Identify the blood parasite species.
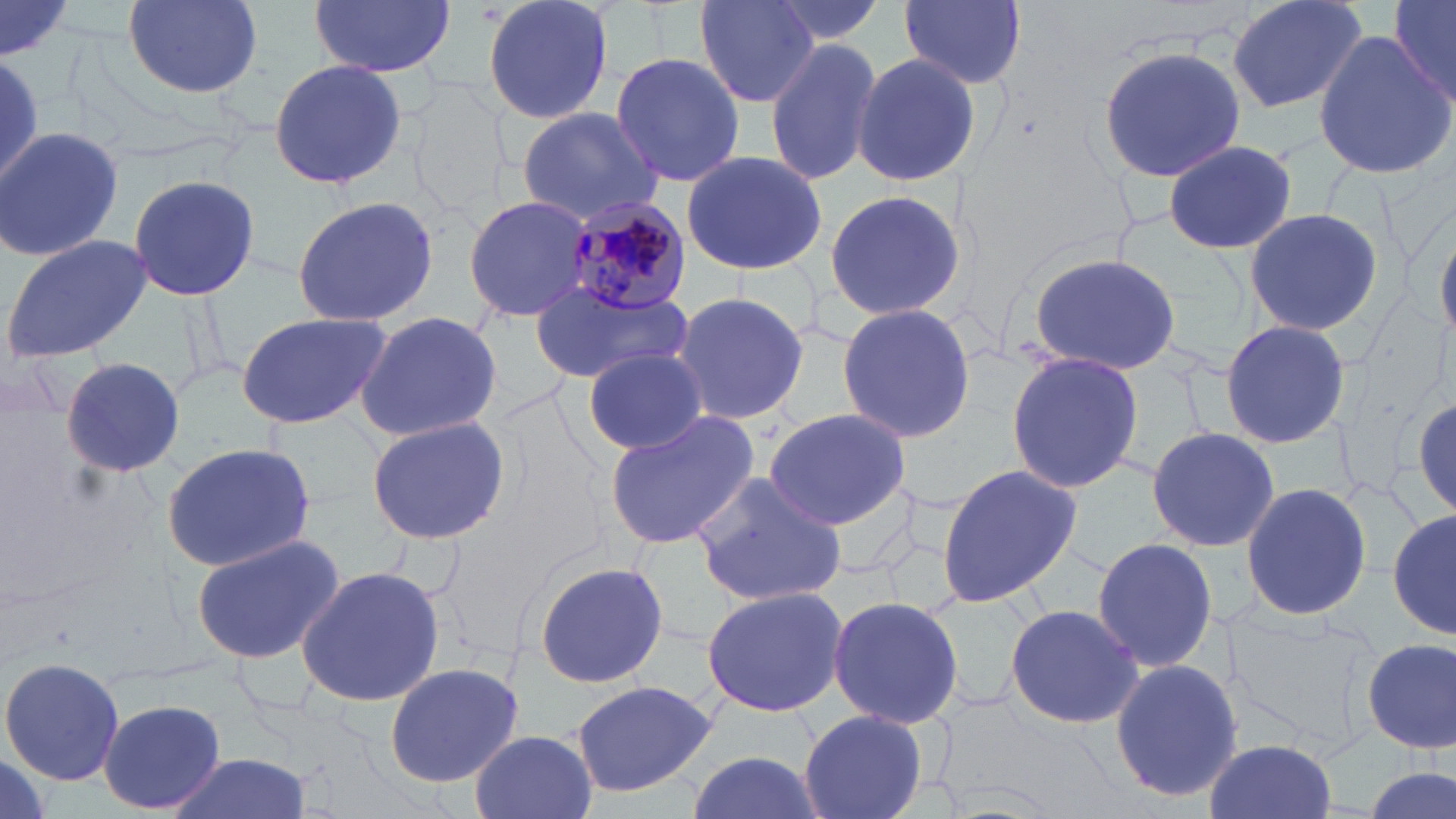

Plasmodium malariae.

Approximate bounding boxes as (x1, y1, x2, y2) in pixels. Plasmodium malariae-infected red blood cell locations: (567, 203, 692, 315). Uninfected red blood cell locations: (481, 0, 616, 127), (763, 0, 888, 48), (900, 0, 1027, 89), (1225, 0, 1372, 115), (1388, 0, 1456, 108), (121, 1, 262, 100), (310, 1, 453, 78), (697, 1, 816, 108), (0, 2, 74, 63), (1313, 32, 1455, 176), (765, 36, 882, 185), (1099, 47, 1246, 180), (609, 50, 744, 186), (851, 53, 984, 188), (266, 59, 407, 191), (515, 104, 663, 226), (1, 126, 125, 263), (1161, 138, 1299, 257), (680, 149, 830, 278), (127, 173, 261, 303), (827, 187, 968, 324), (466, 194, 593, 322), (291, 196, 440, 326), (1241, 206, 1388, 339), (1435, 225, 1455, 342), (1, 235, 153, 363), (1026, 252, 1183, 376), (531, 280, 694, 385), (667, 292, 809, 428), (836, 303, 979, 444), (353, 310, 505, 442), (236, 312, 392, 429), (1220, 319, 1350, 447), (1004, 350, 1146, 492), (583, 351, 709, 453), (61, 358, 186, 476), (1407, 388, 1456, 524), (763, 407, 914, 530), (603, 409, 759, 550), (365, 416, 513, 544), (1144, 426, 1280, 553), (160, 442, 317, 575), (935, 461, 1085, 609), (689, 472, 847, 607), (1240, 481, 1373, 621), (1388, 502, 1455, 643), (188, 532, 346, 665), (1091, 537, 1217, 677), (531, 561, 668, 687), (295, 564, 446, 708), (700, 587, 848, 718), (829, 597, 964, 726), (1225, 602, 1384, 763), (1004, 603, 1143, 729), (1362, 637, 1454, 753), (1, 655, 125, 788), (1106, 658, 1241, 804), (386, 660, 525, 789), (571, 678, 719, 798), (99, 699, 225, 815), (800, 709, 926, 819), (470, 730, 598, 819), (1204, 738, 1341, 819), (684, 750, 822, 819), (166, 753, 311, 819), (1362, 765, 1453, 819). Light microscopy. May-Grünwald-Giemsa stain. Captured at 1000x magnification. Single field of view. Image is 1456×819 pixels. Thin blood film.